Locate and identify every blood parasite.
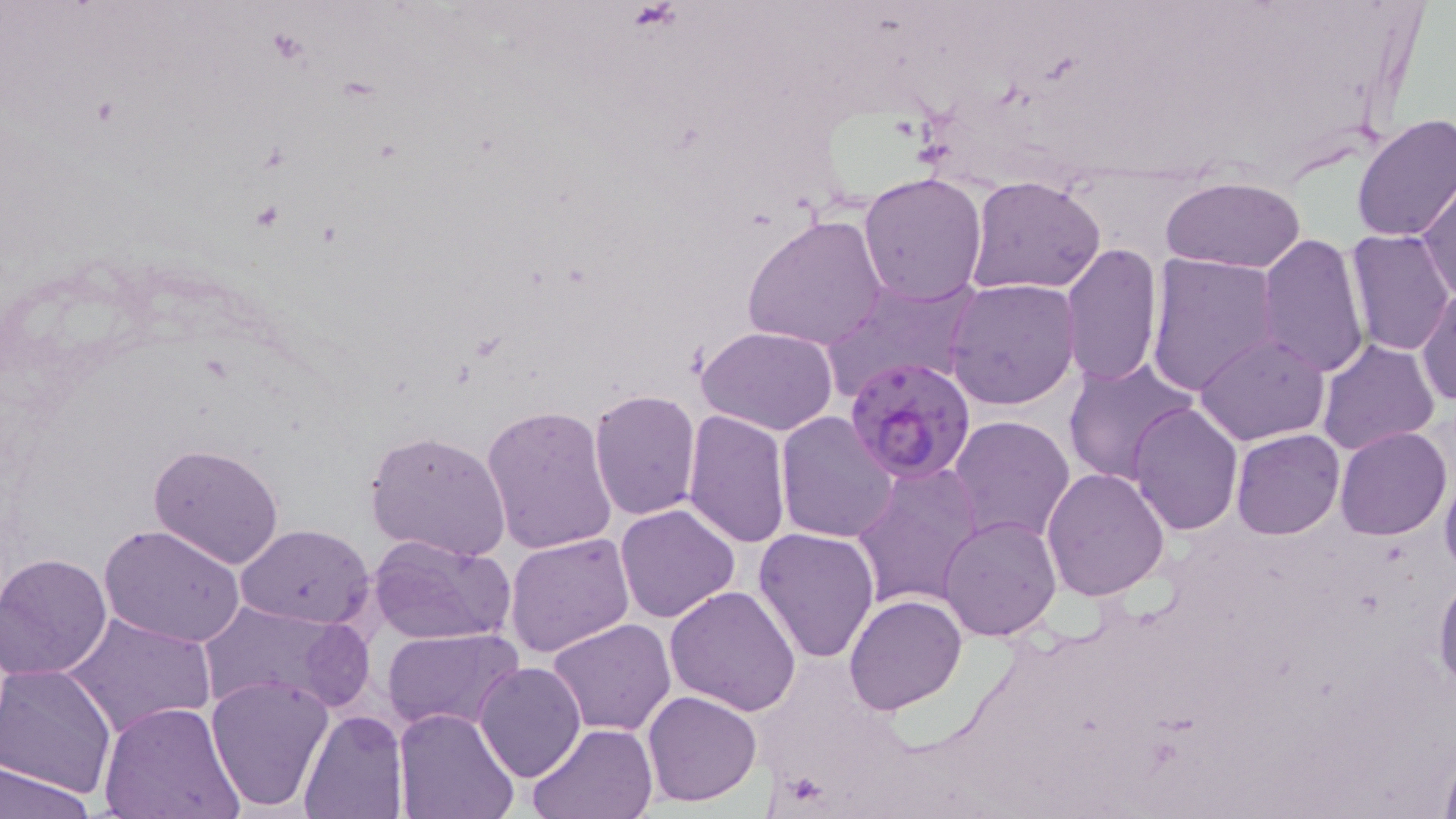
Approximate bounding boxes as (x1, y1, x2, y2) in pixels.
Plasmodium falciparum-infected red blood cells: (844, 356, 977, 483).
No Plasmodium ovale, Plasmodium malariae, Plasmodium vivax, Babesia divergens, or Trypanosoma brucei observed.

{
  "slide_level_diagnosis": "Plasmodium falciparum",
  "field_of_view": "single",
  "stain": "May-Grünwald-Giemsa",
  "magnification": "1000x",
  "preparation": "thin blood film",
  "uninfected_red_blood_cell_locations": "approximate bounding boxes as (x1, y1, x2, y2) in pixels: (1351, 114, 1456, 243), (857, 170, 989, 305), (1159, 175, 1306, 273), (966, 176, 1107, 296), (1417, 180, 1455, 303), (741, 213, 889, 352), (1344, 230, 1453, 357), (1255, 233, 1371, 381), (1060, 241, 1163, 389), (1145, 254, 1282, 397), (820, 275, 982, 401), (945, 278, 1080, 411), (1416, 286, 1456, 410), (696, 324, 840, 436), (1194, 332, 1330, 444), (1315, 339, 1439, 457), (1063, 356, 1201, 487), (588, 389, 701, 520), (1129, 402, 1244, 536), (482, 404, 616, 556), (682, 408, 792, 547), (774, 411, 900, 544), (946, 415, 1075, 547), (1335, 426, 1451, 541), (364, 428, 514, 563), (1231, 429, 1345, 539), (149, 443, 286, 570), (851, 460, 986, 609), (1440, 463, 1456, 583), (1042, 466, 1171, 601), (615, 502, 742, 622), (938, 515, 1063, 642), (237, 523, 375, 629), (99, 524, 247, 648), (753, 527, 880, 664), (504, 532, 635, 658), (369, 533, 518, 644), (1, 552, 116, 681), (1434, 571, 1456, 698), (666, 586, 800, 717), (844, 593, 966, 715), (196, 600, 359, 715), (63, 610, 216, 741), (547, 619, 676, 736), (382, 627, 523, 733), (1, 662, 117, 799), (475, 662, 586, 783), (205, 674, 334, 810), (642, 690, 763, 807), (100, 701, 244, 819), (298, 708, 409, 819), (394, 708, 519, 819), (527, 721, 659, 818), (1436, 752, 1456, 819), (0, 760, 96, 819)",
  "image_size": "1456×819 pixels",
  "modality": "optical microscopy"
}